Report the malaria status of this cell.
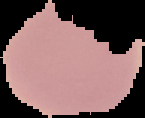

Uninfected.

Image is 145×118 pixels. Segmented cell region on a black background. From a thin blood smear.